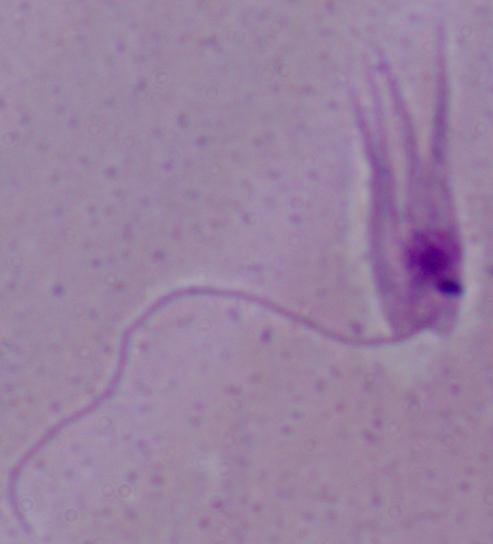
magnification = 1000x
modality = micrograph
identification = Leishmania